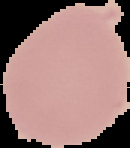
Image is 130×148 pixels. From a thin blood film. Malaria status: uninfected. The area outside the segmented cell region is set to black.